Identify the parasite.
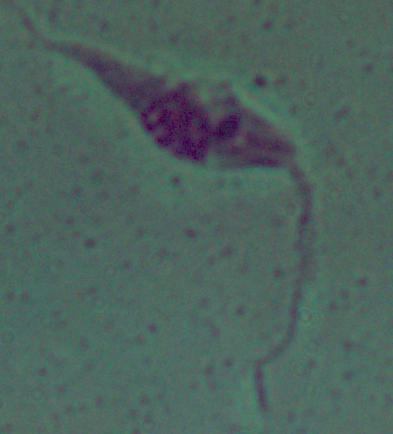

Leishmania.

{
  "magnification": "1000x",
  "modality": "micrograph"
}